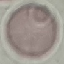
Summary:
  - Malaria status: uninfected
  - Stain: Giemsa
  - Capture: smartphone through the microscope eyepiece
  - Preparation: thin blood film
  - Image type: automatically extracted cell patch, resized to 64 × 64 pixels